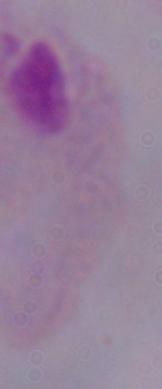
Summary:
  - Modality: micrograph
  - Identification: trichomonad
  - Magnification: 1000x